Comment on the morphology of the erythrocytes.
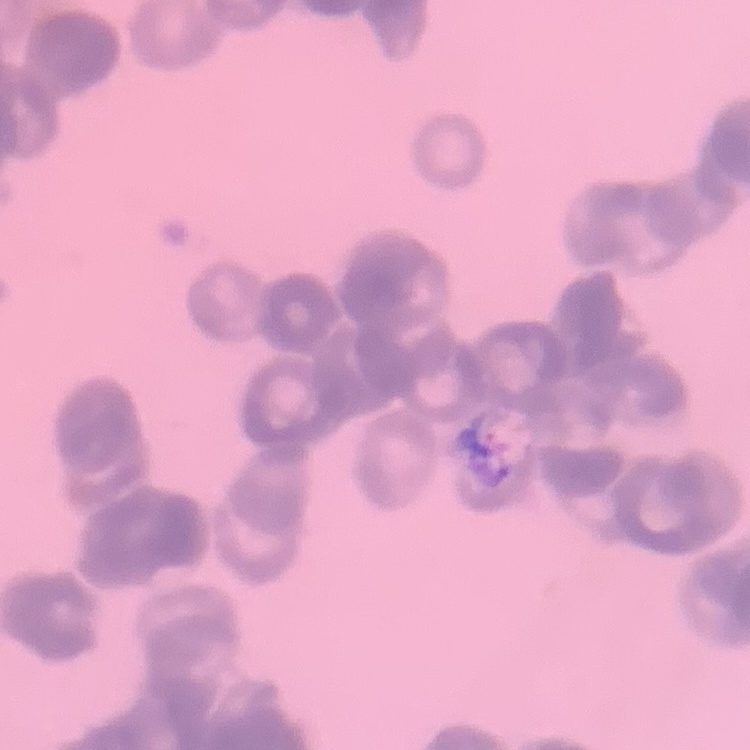
Rouleaux formation.

Stained with either Field's or Giemsa. Square crop of a larger photomicrograph. Thin peripheral smear.